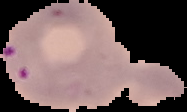
{
  "preparation": "thin blood film",
  "image_type": "segmented cell region on a black background",
  "malaria_status": "parasitized",
  "image_size": "187×112 pixels"
}